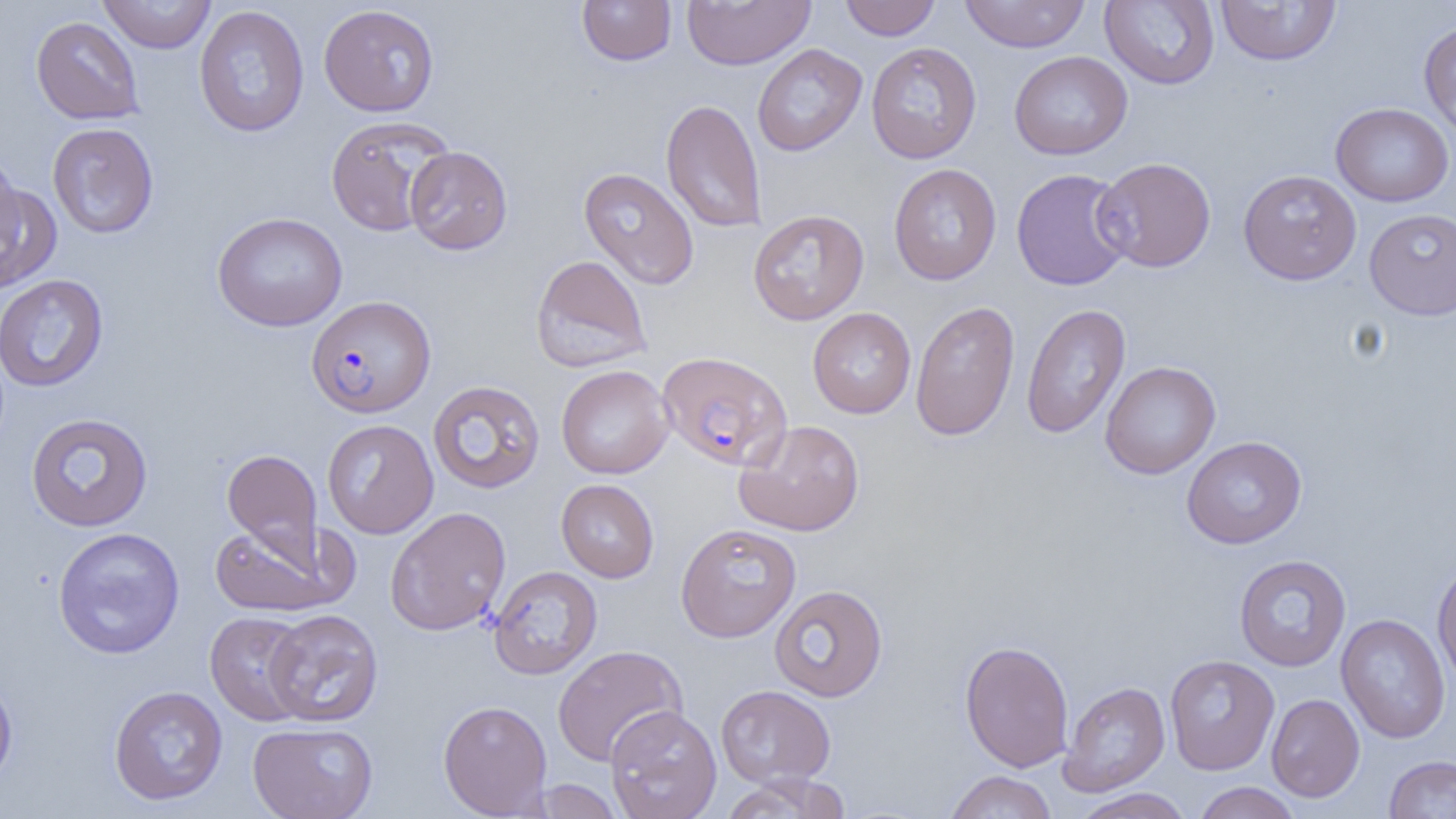

slide-level diagnosis = Plasmodium falciparum
modality = light microscopy
preparation = thin blood film
magnification = 1000x
image size = 1456×819 pixels
uninfected red blood cell locations = approximate bounding boxes as (x1, y1, x2, y2) in pixels: (98, 0, 216, 54), (682, 0, 815, 70), (839, 0, 941, 40), (959, 0, 1091, 53), (576, 1, 677, 66), (1100, 1, 1220, 89), (1214, 1, 1341, 66), (318, 4, 440, 116), (194, 5, 309, 137), (30, 16, 144, 125), (1418, 20, 1456, 141), (865, 42, 982, 164), (752, 44, 867, 157), (1009, 51, 1132, 160), (661, 98, 767, 233), (1331, 102, 1454, 207), (325, 115, 454, 236), (47, 122, 159, 239), (405, 146, 513, 254), (0, 149, 23, 260), (1093, 157, 1216, 272), (888, 163, 1002, 285), (578, 167, 700, 289), (1011, 168, 1133, 291), (1238, 169, 1362, 285), (0, 182, 62, 292), (1364, 208, 1455, 320), (748, 209, 869, 326), (211, 212, 348, 332), (530, 255, 652, 373), (0, 274, 109, 392), (909, 301, 1020, 442), (1021, 303, 1131, 440), (807, 308, 917, 418), (1099, 361, 1221, 479), (556, 364, 674, 479), (428, 380, 546, 494), (25, 413, 154, 532), (322, 419, 439, 539), (734, 419, 865, 537), (1182, 436, 1308, 549), (222, 448, 324, 572), (556, 479, 659, 583), (385, 506, 511, 636), (675, 523, 802, 642), (209, 524, 342, 618), (52, 527, 185, 659), (1233, 554, 1351, 671), (1431, 560, 1456, 689), (488, 565, 602, 680), (769, 584, 888, 702), (264, 609, 384, 728), (204, 611, 313, 726), (1336, 613, 1450, 744), (959, 640, 1074, 772), (552, 645, 688, 766), (1164, 654, 1279, 775), (0, 672, 18, 794), (1059, 680, 1170, 796), (108, 685, 228, 806), (716, 685, 835, 787), (1266, 694, 1365, 802), (438, 699, 553, 818), (605, 705, 721, 819), (248, 722, 377, 819), (1384, 755, 1456, 818), (944, 771, 1057, 819), (719, 773, 852, 819), (528, 778, 624, 818), (1192, 782, 1302, 819), (1070, 788, 1195, 819)
field of view = single
Plasmodium falciparum-infected red blood cell locations = approximate bounding boxes as (x1, y1, x2, y2) in pixels: (306, 295, 436, 418), (657, 350, 792, 472)